Comment on the morphology of the red blood cells.
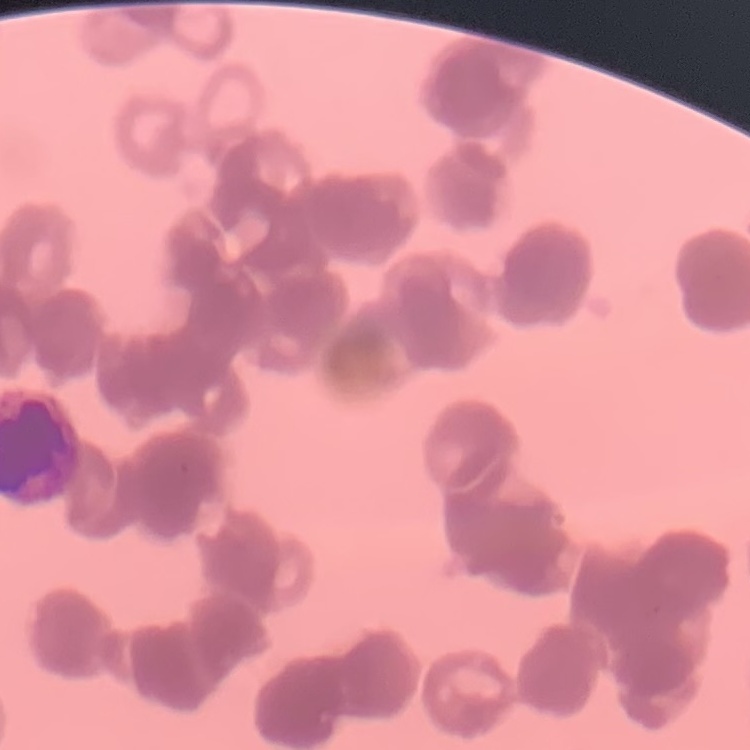

They show rouleaux formation.

One tile cut from a larger photomicrograph. Thin peripheral smear. Stained with either Field's or Giemsa.